Classify this cell by malaria status.
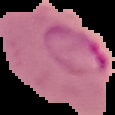

It is parasitized.

Summary:
  - Image type: segmented cell region with the area outside set to black
  - Image size: 115×115 pixels
  - Preparation: thin blood film